Name the parasite shown.
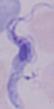
This is a trypanosome.

Summary:
  - Magnification: 1000x
  - Modality: micrograph